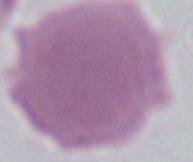

Summary:
  - Magnification: 1000x
  - Identification: red blood cell
  - Modality: micrograph